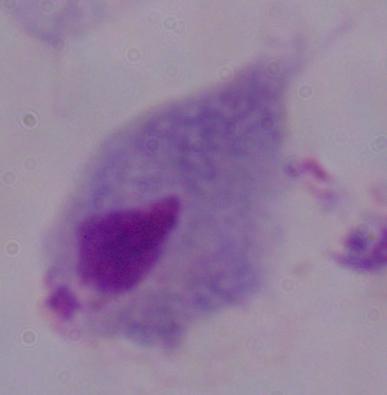

Summary:
  - Magnification: 1000x
  - Identification: trichomonad
  - Modality: micrograph